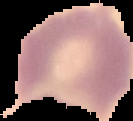

Summary:
  - Preparation: thin blood smear
  - Malaria status: uninfected
  - Image size: 133×121 pixels
  - Image type: cell region segmented out of the field of view; surrounding area masked to black